Assess this cell for malaria.
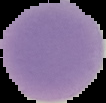
Uninfected.

From a thin blood film. Segmented cell region on a black background. Image is 106×103 pixels.